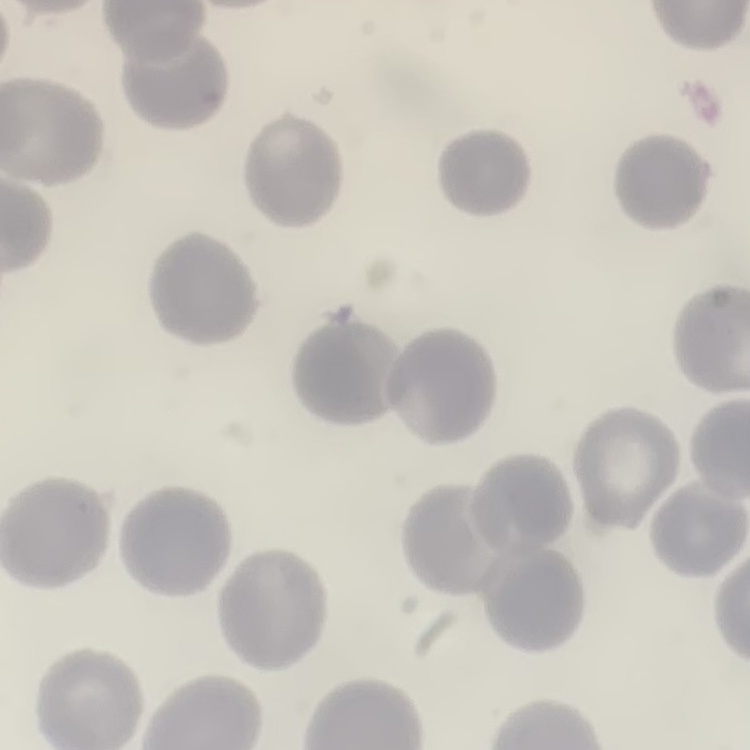
The red blood cells exhibit no rouleaux formation. Square crop of a larger photomicrograph. Stained with either Field's or Giemsa. Thin peripheral smear.